Identify the parasite.
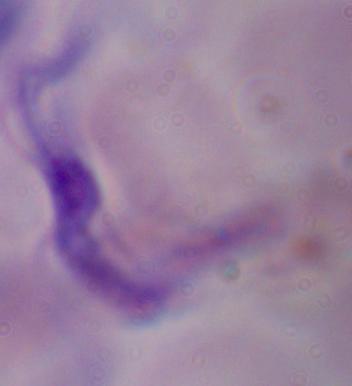
A trypanosome.

modality: photomicrograph
magnification: 1000x